Locate and identify every blood parasite.
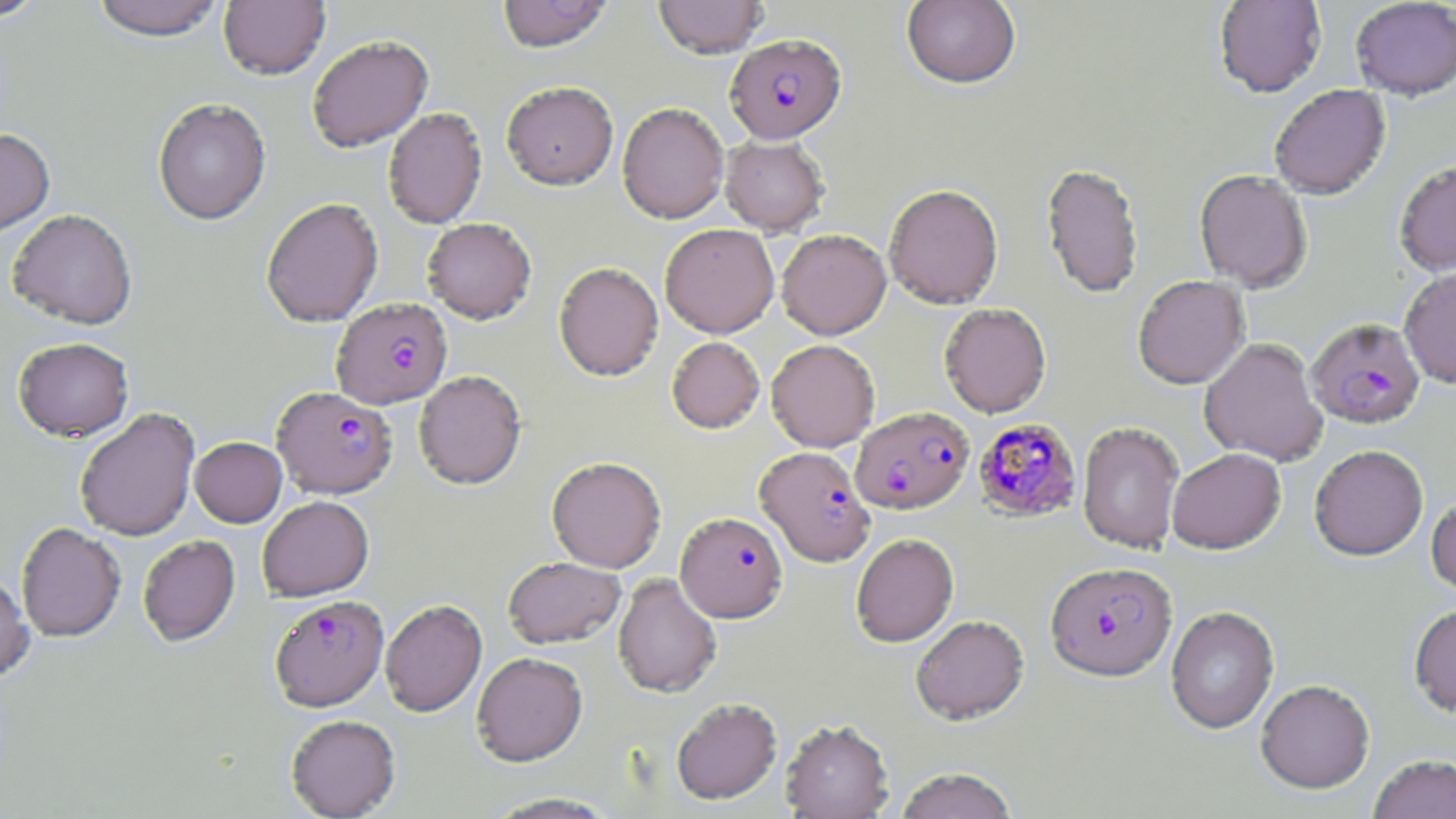

Approximate bounding boxes as [x1, y1, x2, y2] in pixels.
Plasmodium falciparum-infected red blood cells: [725, 33, 846, 143], [332, 297, 453, 409], [1306, 318, 1425, 431], [272, 386, 397, 498], [852, 406, 974, 514], [973, 418, 1082, 523], [755, 446, 875, 567], [675, 512, 787, 622], [1045, 561, 1176, 681], [270, 594, 388, 710].
No Plasmodium ovale, Plasmodium malariae, Plasmodium vivax, Babesia divergens, or Trypanosoma brucei observed.

Uninfected red blood cell locations: [0, 0, 50, 22], [90, 0, 227, 40], [218, 0, 330, 80], [496, 0, 614, 53], [654, 0, 768, 58], [901, 0, 1021, 90], [1213, 0, 1327, 98], [1351, 1, 1456, 101], [306, 34, 433, 152], [501, 81, 618, 190], [1269, 85, 1391, 201], [152, 97, 271, 225], [617, 102, 729, 224], [383, 107, 487, 229], [0, 128, 55, 236], [720, 134, 829, 235], [1394, 160, 1456, 278], [1040, 163, 1144, 300], [1194, 170, 1312, 292], [883, 184, 1004, 309], [261, 197, 383, 327], [7, 208, 137, 329], [422, 217, 537, 323], [660, 223, 779, 338], [777, 229, 891, 340], [553, 261, 664, 381], [1399, 268, 1456, 389], [1132, 275, 1250, 389], [938, 303, 1051, 417], [667, 336, 765, 433], [12, 337, 134, 441], [1199, 337, 1328, 466], [766, 339, 880, 452], [414, 370, 527, 488], [74, 407, 200, 541], [1077, 421, 1185, 554], [190, 436, 286, 527], [1309, 445, 1429, 561], [1166, 447, 1286, 554], [546, 456, 666, 572], [1426, 493, 1456, 600], [258, 495, 374, 601], [16, 522, 125, 641], [851, 533, 959, 648], [138, 535, 240, 646], [502, 557, 625, 649], [0, 573, 34, 682], [613, 573, 722, 698], [380, 599, 487, 717], [1409, 601, 1456, 719], [1165, 606, 1280, 734], [911, 614, 1029, 724], [471, 651, 588, 766], [1255, 679, 1375, 794], [671, 697, 782, 804], [285, 714, 400, 818], [780, 718, 894, 818], [1367, 754, 1456, 818], [894, 767, 1019, 819], [482, 793, 621, 818]. Slide-level diagnosis: Plasmodium falciparum. Thin blood film. Image is 1456×819 pixels. Single field of view. Captured at 1000x magnification. Optical microscopy. May-Grünwald-Giemsa stain.